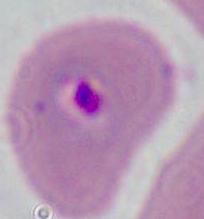
Photomicrograph. 400x or 1000x magnification. A Plasmodium parasite is seen.